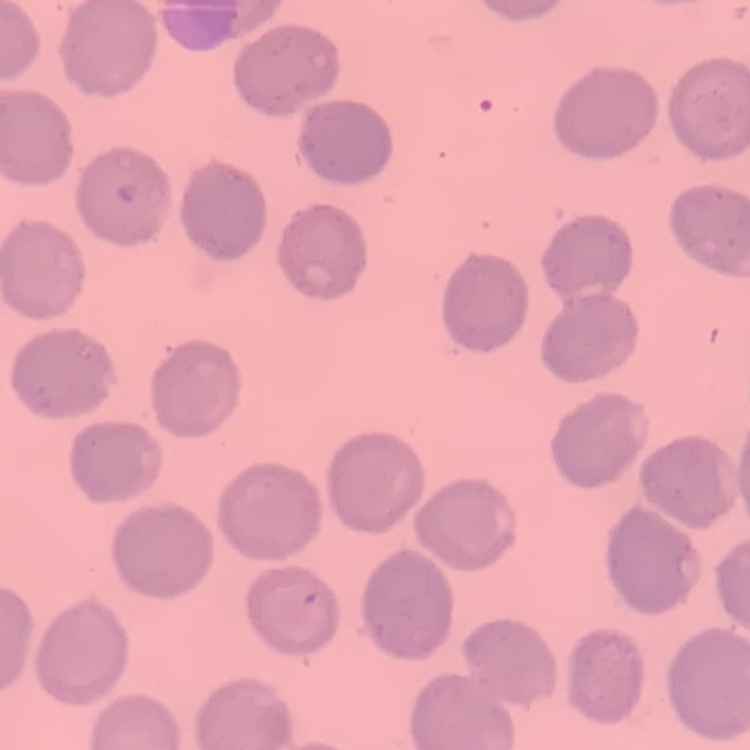

erythrocyte morphology = no rouleaux formation
image type = square crop of a larger photomicrograph
stain = Field's or Giemsa
preparation = thin peripheral smear